Report the malaria status of this cell.
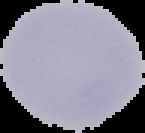

Uninfected.

image type = cell region segmented out of the field of view; surrounding area masked to black
image size = 145×133 pixels
preparation = thin blood smear